Assess this cell for malaria.
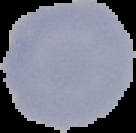
Uninfected.

Segmented cell region on a black background. Image is 136×133 pixels. From a thin blood smear.